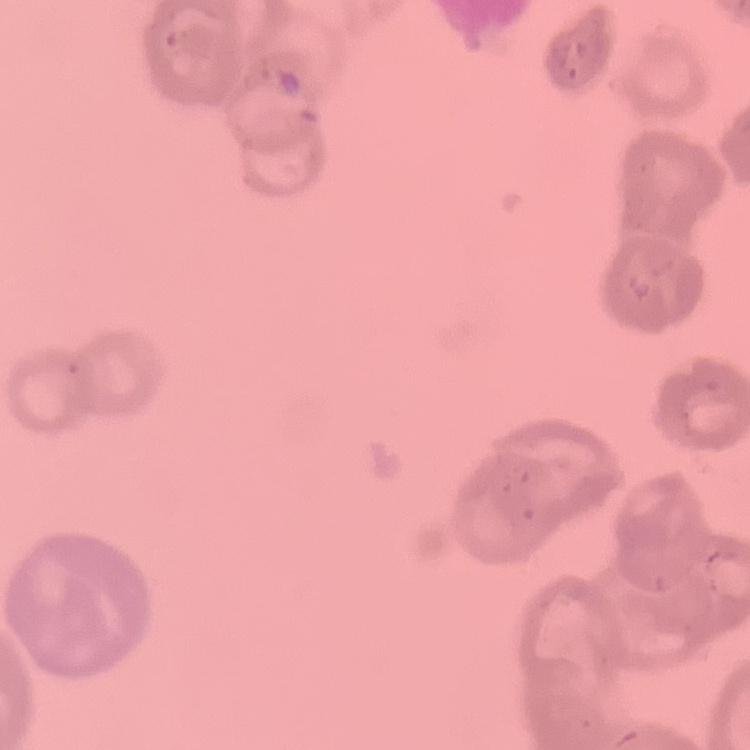

The erythrocytes show rouleaux formation. One tile cut from a larger photomicrograph. Thin peripheral smear. Stained with either Field's or Giemsa.